Give the extent of all uninfected red blood cells.
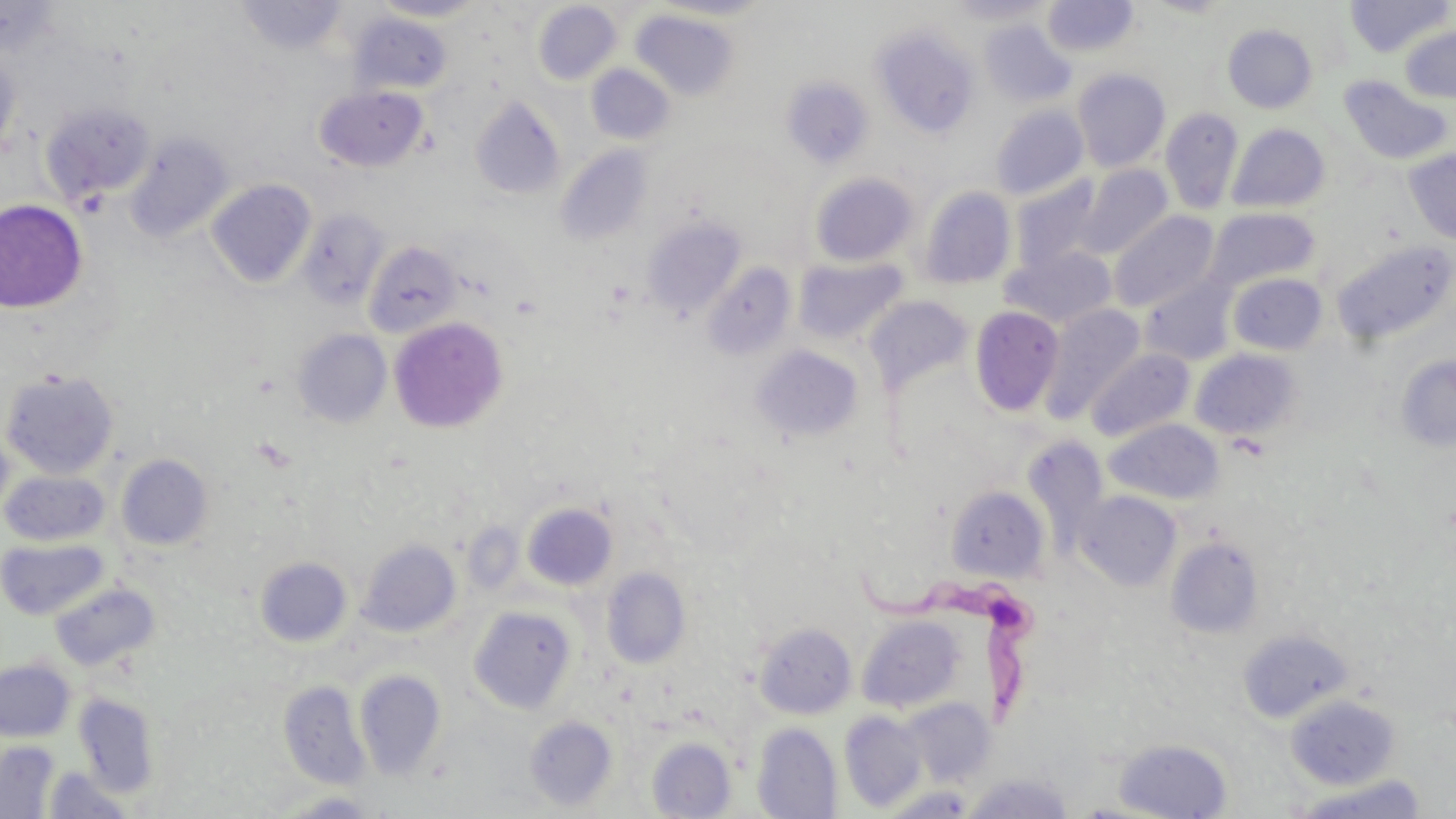
Approximate bounding boxes as (x1,y1)-(x2,y2) corner pairs in pixels.
Uninfected red blood cells: (0,0)-(64,59), (370,0)-(489,22), (651,0)-(777,21), (944,0)-(1056,25), (1145,0)-(1238,18), (1345,0)-(1453,57), (236,1)-(348,55), (1042,1)-(1139,57), (533,2)-(621,85), (630,9)-(740,101), (350,13)-(453,96), (979,20)-(1076,108), (1222,24)-(1317,113), (871,25)-(982,139), (1400,26)-(1456,104), (0,45)-(22,162), (586,64)-(675,145), (1072,67)-(1171,172), (1338,75)-(1453,166), (782,77)-(873,168), (314,86)-(429,172), (470,95)-(565,200), (41,101)-(156,207), (990,105)-(1088,201), (1160,108)-(1243,214), (1227,123)-(1330,214), (124,132)-(234,244), (556,145)-(652,246), (1403,149)-(1456,245), (1073,166)-(1172,260), (810,172)-(918,267), (1010,177)-(1105,274), (206,179)-(316,289), (918,186)-(1016,289), (0,200)-(88,313), (1206,207)-(1320,291), (296,209)-(390,310), (1109,210)-(1219,312), (643,218)-(745,317), (1332,239)-(1455,346), (362,241)-(463,340), (1002,246)-(1116,328), (794,257)-(906,345), (702,262)-(797,361), (1228,272)-(1328,355), (1141,276)-(1236,366), (864,295)-(974,397), (1041,303)-(1145,421), (969,306)-(1064,417), (389,316)-(508,433), (293,329)-(392,428), (751,344)-(865,445), (1085,348)-(1194,442), (1190,349)-(1303,442), (1396,355)-(1456,452), (1,369)-(120,480), (1106,419)-(1223,505), (0,424)-(15,523), (116,453)-(214,551), (1,470)-(110,546), (946,485)-(1048,582), (1075,490)-(1181,590), (523,503)-(618,591), (1166,535)-(1265,640), (1,538)-(110,620), (357,538)-(461,638), (255,556)-(353,647), (601,566)-(691,669), (50,581)-(160,672), (468,605)-(577,714), (856,615)-(966,712), (754,622)-(857,719), (1238,628)-(1354,723), (0,658)-(76,742), (354,669)-(446,780), (279,681)-(370,788), (74,693)-(161,797), (1285,694)-(1400,788), (903,698)-(995,786), (839,711)-(927,812), (525,716)-(617,812), (751,722)-(843,819), (646,736)-(737,818), (1112,737)-(1233,818), (0,740)-(60,818), (42,766)-(136,818), (963,771)-(1074,818), (1288,774)-(1431,818), (879,786)-(978,818), (272,791)-(384,818).

Summary:
  - Trypanosoma brucei locations: (857,570)-(1046,730)
  - Slide-level diagnosis: Trypanosoma brucei
  - Preparation: thin blood film
  - Modality: optical microscopy
  - Magnification: 1000x
  - Image size: 1456×819 pixels
  - Field of view: one of a larger specimen
  - Stain: May-Grünwald-Giemsa